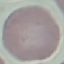

result: negative for malaria parasites
image_type: cell patch, automatically extracted from a larger field of view and resized to 64 × 64 pixels
stain: Giemsa
capture: smartphone camera at the microscope eyepiece
preparation: thin smear